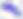

Summary:
  - Identification: Toxoplasma gondii
  - Modality: micrograph
  - Magnification: 400x